Assess this cell for malaria.
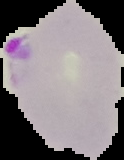
It is parasitized.

Summary:
  - Image size: 124×160 pixels
  - Image type: cell region segmented out of the field of view; surrounding area masked to black
  - Preparation: thin blood film